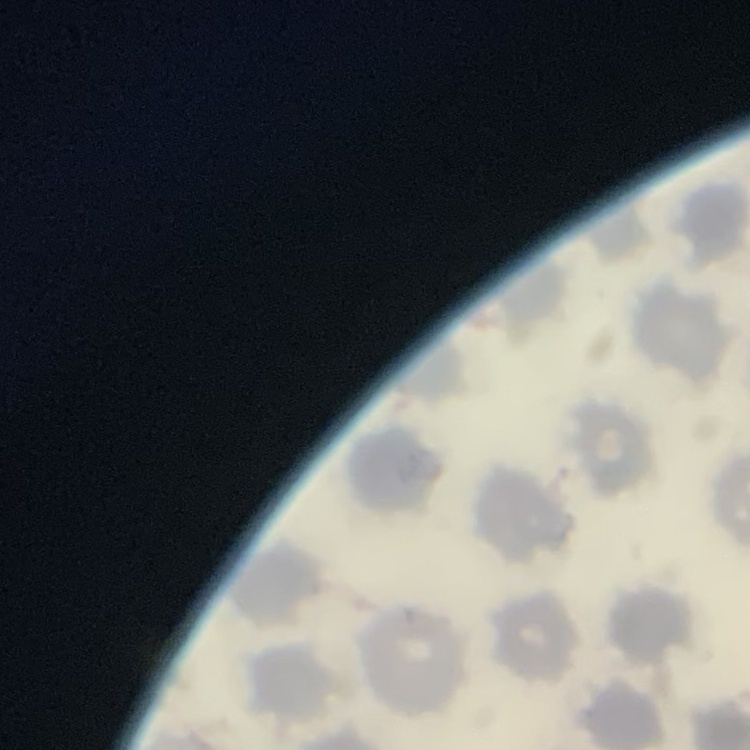

red_blood_cell_morphology: no rouleaux formation
preparation: thin peripheral smear
image_type: square crop of a larger photomicrograph
stain: Field's or Giemsa